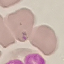

Summary:
  - Result: negative for malaria parasites
  - Image type: automatically extracted cell patch, resized to 64 × 64 pixels
  - Preparation: thin blood film
  - Stain: Giemsa
  - Capture: smartphone camera at the microscope eyepiece